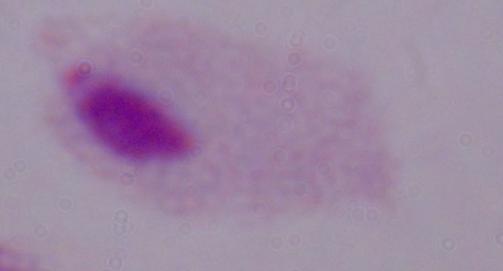

1000x magnification. A trichomonad is shown. Micrograph.